Report the malaria status of this cell.
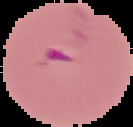

Parasitized.

image type = segmented cell region with the area outside set to black
preparation = thin blood smear
image size = 133×127 pixels